Assess the morphology of the red blood cells.
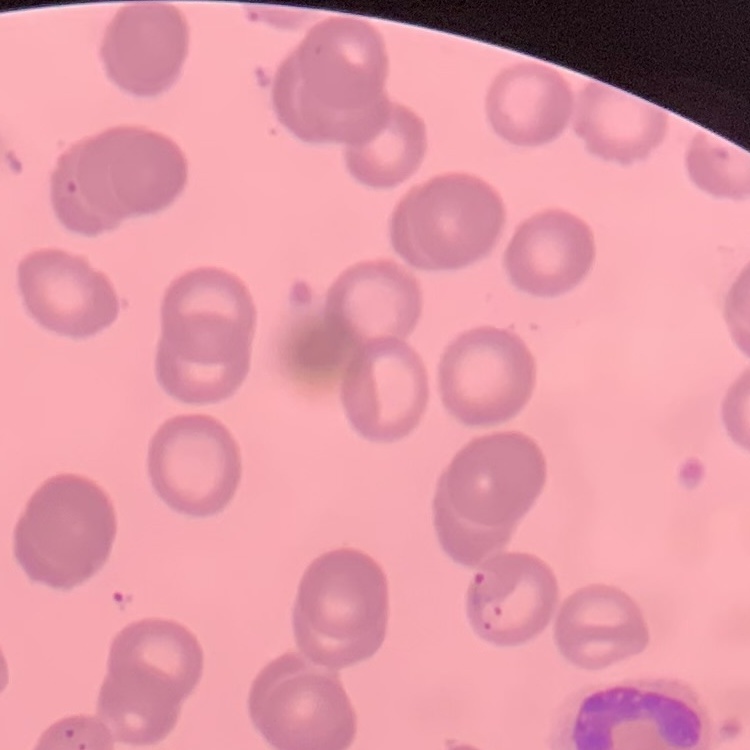

No rouleaux formation.

One tile cut from a larger photomicrograph. Thin peripheral smear. Stained with either Field's or Giemsa.